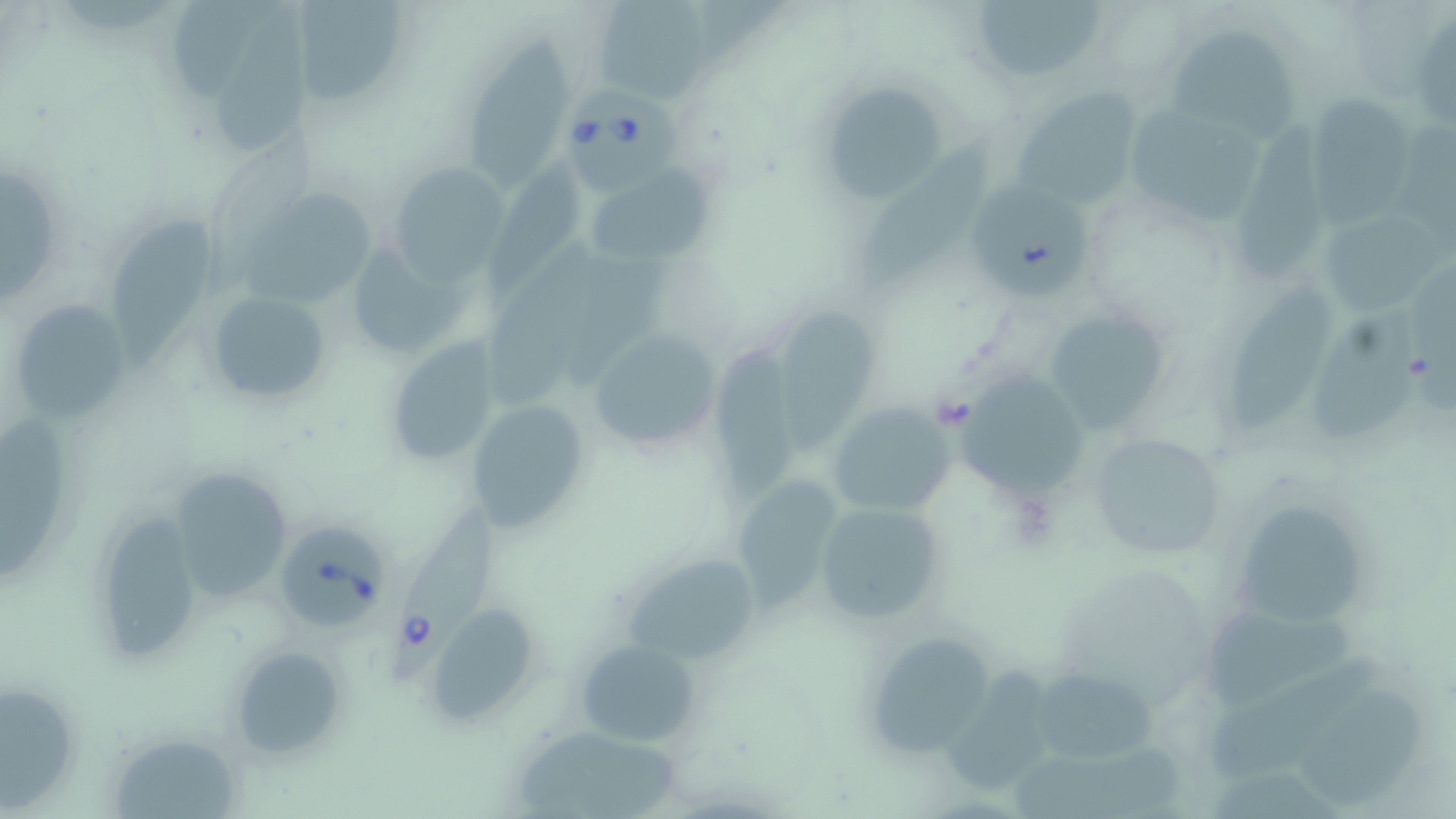
Approximate bounding boxes as (x1, y1, x2, y2) in pixels. Babesia divergens-infected red blood cell locations: (557, 81, 694, 188), (385, 514, 494, 690), (280, 523, 390, 627). Uninfected red blood cell locations: (170, 0, 266, 109), (291, 0, 413, 108), (591, 0, 715, 102), (972, 0, 1104, 86), (215, 9, 307, 148), (1411, 10, 1456, 129), (1165, 24, 1302, 142), (468, 29, 563, 193), (816, 77, 955, 204), (1015, 91, 1140, 207), (1306, 95, 1419, 219), (1120, 102, 1267, 226), (1237, 117, 1335, 283), (858, 135, 993, 294), (483, 160, 584, 302), (386, 164, 513, 281), (583, 166, 706, 269), (0, 167, 57, 299), (977, 183, 1094, 297), (248, 188, 374, 304), (1322, 210, 1452, 319), (109, 213, 214, 363), (351, 240, 472, 353), (487, 243, 606, 409), (1231, 278, 1333, 433), (205, 289, 335, 408), (7, 299, 131, 423), (1312, 307, 1425, 440), (1038, 308, 1174, 434), (783, 311, 874, 456), (586, 328, 721, 456), (384, 337, 505, 465), (710, 340, 809, 503), (954, 375, 1088, 496), (468, 399, 591, 534), (826, 400, 955, 518), (1088, 432, 1226, 561), (160, 465, 297, 602), (737, 475, 840, 612), (812, 499, 949, 626), (1240, 500, 1360, 624), (88, 508, 207, 661), (620, 549, 766, 666), (1201, 601, 1360, 702), (428, 604, 540, 723), (858, 630, 998, 760), (576, 640, 699, 747), (229, 645, 349, 759), (952, 656, 1053, 794), (1210, 660, 1394, 775), (1028, 665, 1163, 767), (1301, 680, 1424, 809), (0, 682, 82, 810), (518, 727, 688, 816), (110, 730, 242, 818). Slide-level diagnosis: Babesia divergens. Single field of view. Image is 1456×819 pixels. May-Grünwald-Giemsa stain. Optical microscopy. Thin blood smear. Captured at 1000x magnification.